Find each parasitized red blood cell.
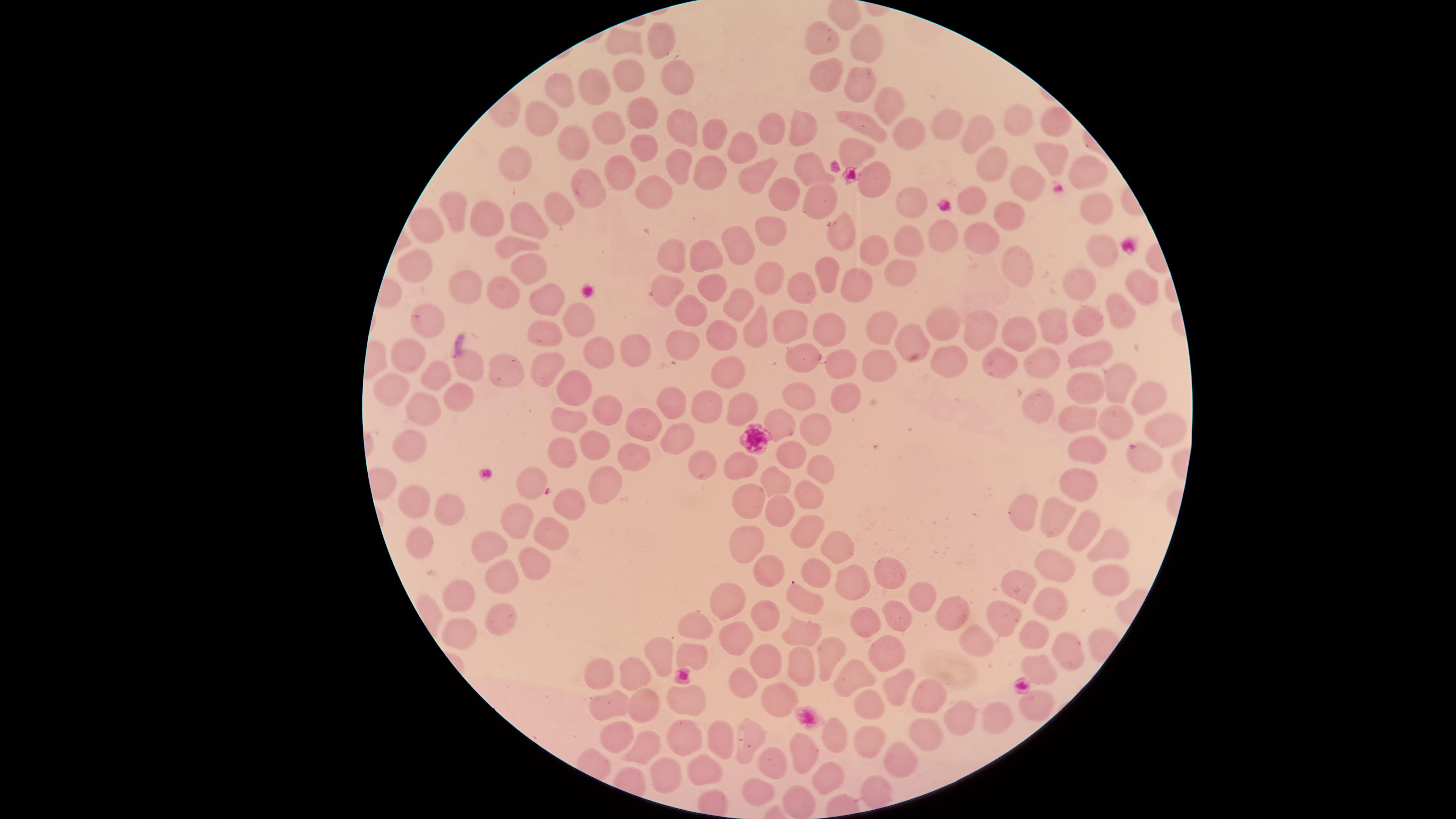
No parasitized red blood cells identified.

Approximate marker points, in pixels from the top-left corner. Uninfected red blood cells: (x=664, y=37), (x=828, y=38), (x=626, y=42), (x=867, y=48), (x=632, y=73), (x=825, y=75), (x=672, y=77), (x=851, y=80), (x=598, y=90), (x=567, y=91), (x=883, y=107), (x=644, y=111), (x=544, y=117), (x=947, y=121), (x=610, y=123), (x=1022, y=123), (x=777, y=124), (x=1053, y=124), (x=870, y=129), (x=799, y=130), (x=676, y=131), (x=709, y=131), (x=901, y=135), (x=978, y=135), (x=575, y=139), (x=644, y=145), (x=748, y=145), (x=857, y=150), (x=1052, y=156), (x=515, y=157), (x=997, y=164), (x=680, y=168), (x=705, y=171), (x=1080, y=171), (x=806, y=172), (x=876, y=175), (x=612, y=176), (x=760, y=178), (x=1030, y=186), (x=586, y=190), (x=653, y=191), (x=785, y=196), (x=906, y=197), (x=821, y=200), (x=968, y=201), (x=559, y=207), (x=457, y=210), (x=1095, y=212), (x=494, y=214), (x=1007, y=215), (x=531, y=223), (x=426, y=227), (x=770, y=233), (x=839, y=233), (x=908, y=236), (x=947, y=236), (x=983, y=238), (x=738, y=239), (x=508, y=244), (x=1098, y=245), (x=712, y=255), (x=872, y=256), (x=673, y=257), (x=416, y=261), (x=1010, y=261), (x=527, y=268), (x=898, y=272), (x=766, y=275), (x=827, y=276), (x=847, y=280), (x=713, y=281), (x=464, y=282), (x=1079, y=283), (x=806, y=285), (x=660, y=287), (x=1142, y=288), (x=503, y=292), (x=547, y=294), (x=746, y=303), (x=689, y=308), (x=1124, y=308), (x=572, y=318), (x=1059, y=318), (x=1092, y=318), (x=426, y=322), (x=937, y=322), (x=789, y=324), (x=829, y=324), (x=987, y=326), (x=761, y=327), (x=882, y=328), (x=1026, y=331), (x=547, y=337), (x=725, y=337), (x=921, y=337), (x=676, y=340), (x=638, y=345), (x=806, y=353), (x=406, y=355), (x=1088, y=357), (x=599, y=358), (x=1004, y=358), (x=460, y=360), (x=943, y=364), (x=843, y=365), (x=1044, y=365), (x=875, y=366), (x=553, y=368), (x=503, y=369), (x=434, y=373), (x=723, y=373), (x=402, y=381), (x=1124, y=385), (x=583, y=388), (x=846, y=390), (x=1089, y=392), (x=665, y=397), (x=463, y=399), (x=792, y=399), (x=1153, y=400), (x=1044, y=402), (x=709, y=406), (x=608, y=409), (x=741, y=409), (x=426, y=412), (x=571, y=420), (x=785, y=421), (x=651, y=424), (x=1088, y=424), (x=1113, y=425), (x=813, y=428), (x=682, y=438), (x=597, y=441), (x=413, y=445), (x=564, y=446), (x=1080, y=452), (x=790, y=456), (x=636, y=457), (x=1137, y=457), (x=740, y=468), (x=822, y=468), (x=700, y=475), (x=781, y=478), (x=1080, y=478), (x=604, y=485), (x=529, y=490), (x=799, y=496), (x=753, y=497), (x=410, y=500), (x=567, y=506), (x=450, y=508), (x=1017, y=511), (x=785, y=512), (x=1048, y=518), (x=516, y=521), (x=802, y=530), (x=1086, y=530), (x=547, y=533), (x=419, y=542), (x=752, y=543), (x=834, y=545), (x=1100, y=547), (x=485, y=557), (x=530, y=564), (x=824, y=569), (x=1056, y=569), (x=771, y=572), (x=1107, y=578), (x=500, y=579), (x=850, y=580), (x=897, y=580), (x=1021, y=592), (x=917, y=599), (x=450, y=602), (x=1052, y=602), (x=809, y=605), (x=734, y=608), (x=760, y=613), (x=501, y=614), (x=894, y=614), (x=952, y=616), (x=1013, y=619), (x=692, y=622), (x=864, y=624), (x=456, y=631), (x=798, y=634), (x=1034, y=638), (x=734, y=640), (x=971, y=645), (x=663, y=648), (x=827, y=650), (x=1063, y=650), (x=882, y=652), (x=695, y=654), (x=768, y=663), (x=804, y=665), (x=1037, y=673), (x=607, y=678), (x=637, y=679), (x=739, y=679), (x=858, y=681), (x=891, y=689), (x=933, y=698), (x=773, y=699), (x=692, y=702), (x=646, y=705), (x=611, y=709), (x=1040, y=709), (x=870, y=713), (x=997, y=715), (x=961, y=717), (x=618, y=734), (x=674, y=735), (x=923, y=737), (x=834, y=738), (x=722, y=739), (x=870, y=740), (x=641, y=746), (x=743, y=746), (x=803, y=750), (x=894, y=757), (x=772, y=765), (x=701, y=768), (x=822, y=774), (x=664, y=776), (x=760, y=792), (x=876, y=796), (x=804, y=804). Circular visible region. Thin smear of blood. One field of view of the specimen. Photographed with a smartphone camera through the microscope eyepiece. Image is 1456×819 pixels. Giemsa-stained preparation.